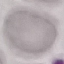
result = no malaria parasites seen
preparation = thin blood film
image type = automatically extracted cell patch, resized to 64 × 64 pixels
stain = Giemsa
capture = smartphone through the microscope eyepiece